Give the position of every Plasmodium parasite visible.
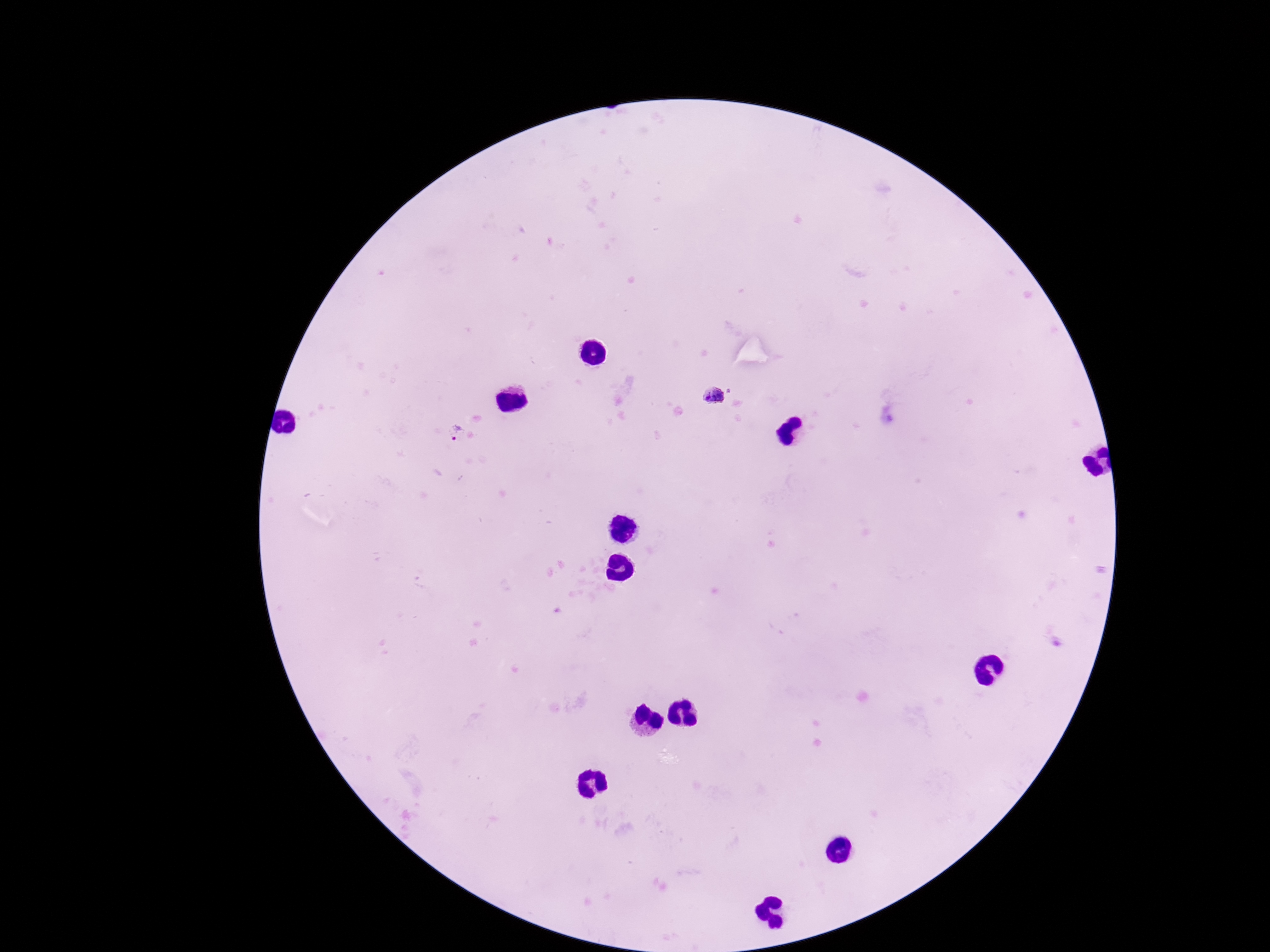

Approximate centers as [x, y] in pixels.
Plasmodium parasites: [713, 396], [454, 436].

{
  "capture": "smartphone camera through the microscope eyepiece",
  "magnification": "100x",
  "patient_malaria_status": "positive",
  "stain": "Giemsa",
  "image_size": "1270×952 pixels",
  "preparation": "thick blood film",
  "field_of_view": "one from this slide"
}